Assess for Plasmodium parasites.
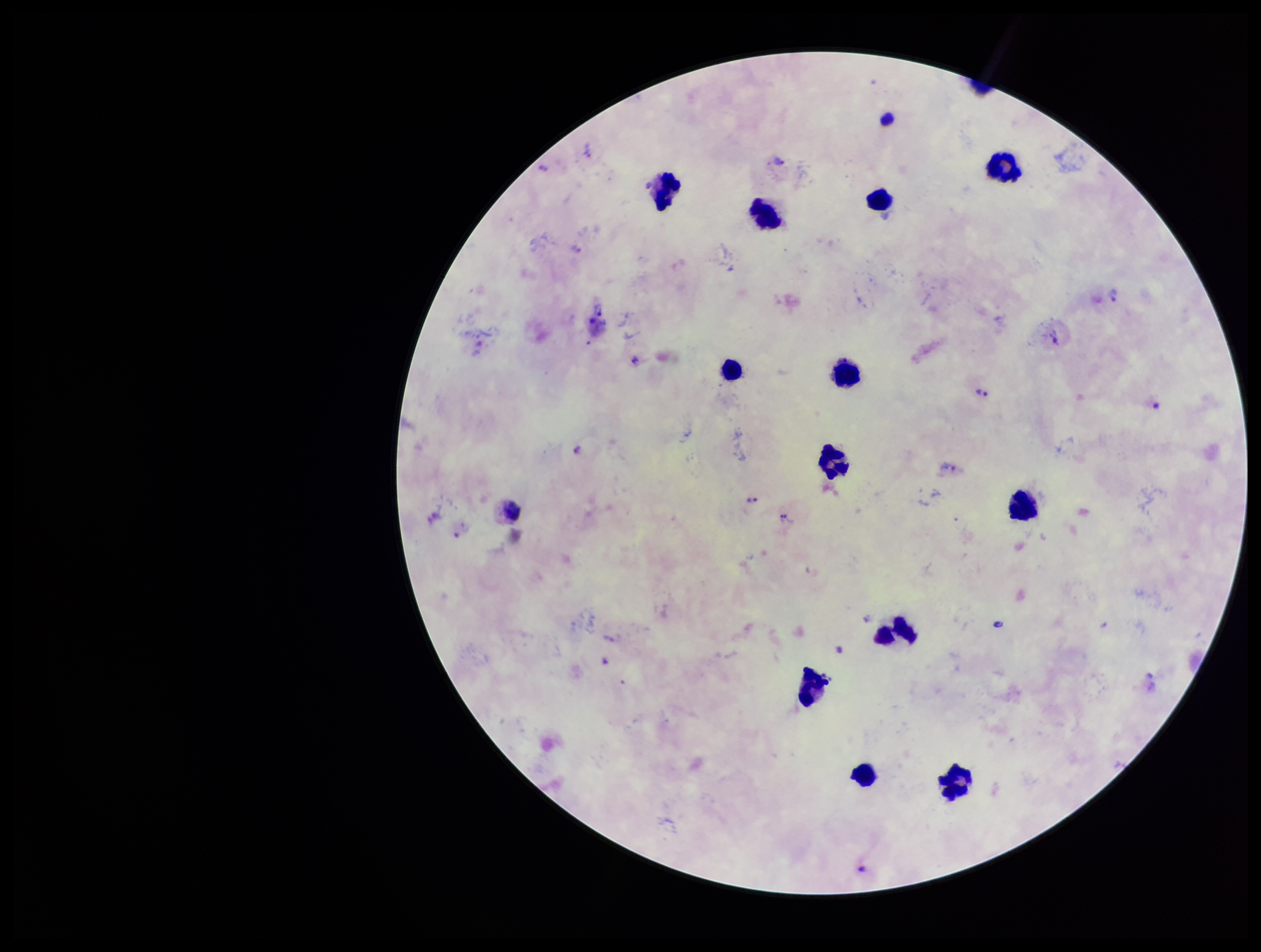
Detected.

Summary:
  - Stain: Giemsa
  - Species reported for this patient: Plasmodium vivax
  - Patient malaria status: infected
  - Leukocyte count: 14
  - Parasite count: 14
  - Capture: smartphone photograph through the microscope eyepiece
  - Field of view: single
  - Image size: 1261×952 pixels
  - Preparation: thick blood smear